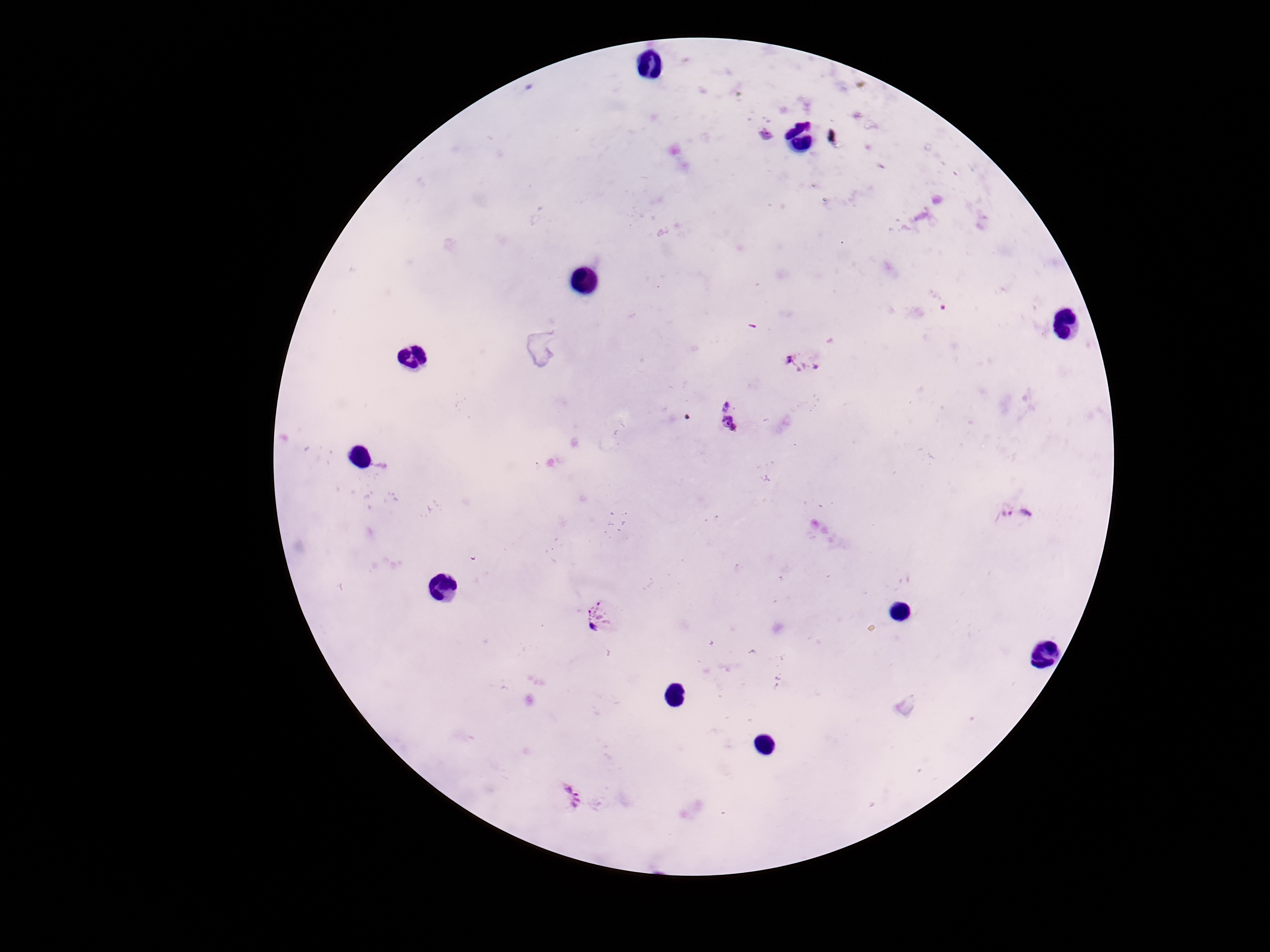
Approximate centers as (x, y) in pixels. Plasmodium parasite locations: (766, 135), (804, 364), (729, 419), (1017, 513), (597, 618), (565, 799). Giemsa-stained preparation. Smartphone photograph taken through the microscope eyepiece. Image is 1270×952 pixels. 100x magnification. Thick peripheral-blood smear. One field from this slide. Patient malaria status: positive.